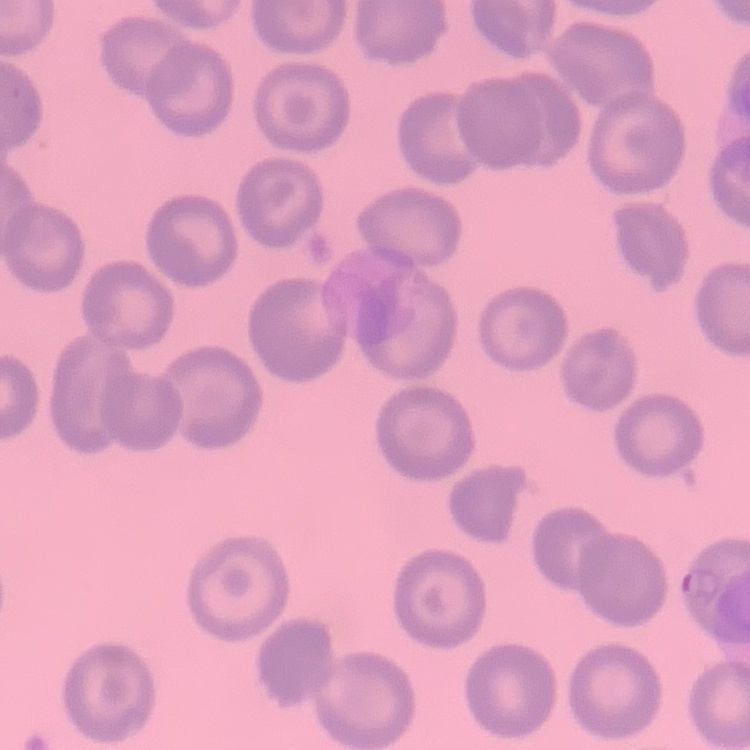

erythrocyte morphology = no rouleaux formation
stain = Field's or Giemsa
preparation = thin peripheral smear
image type = one tile cut from a larger photomicrograph